Locate every Plasmodium ovale-infected red blood cell.
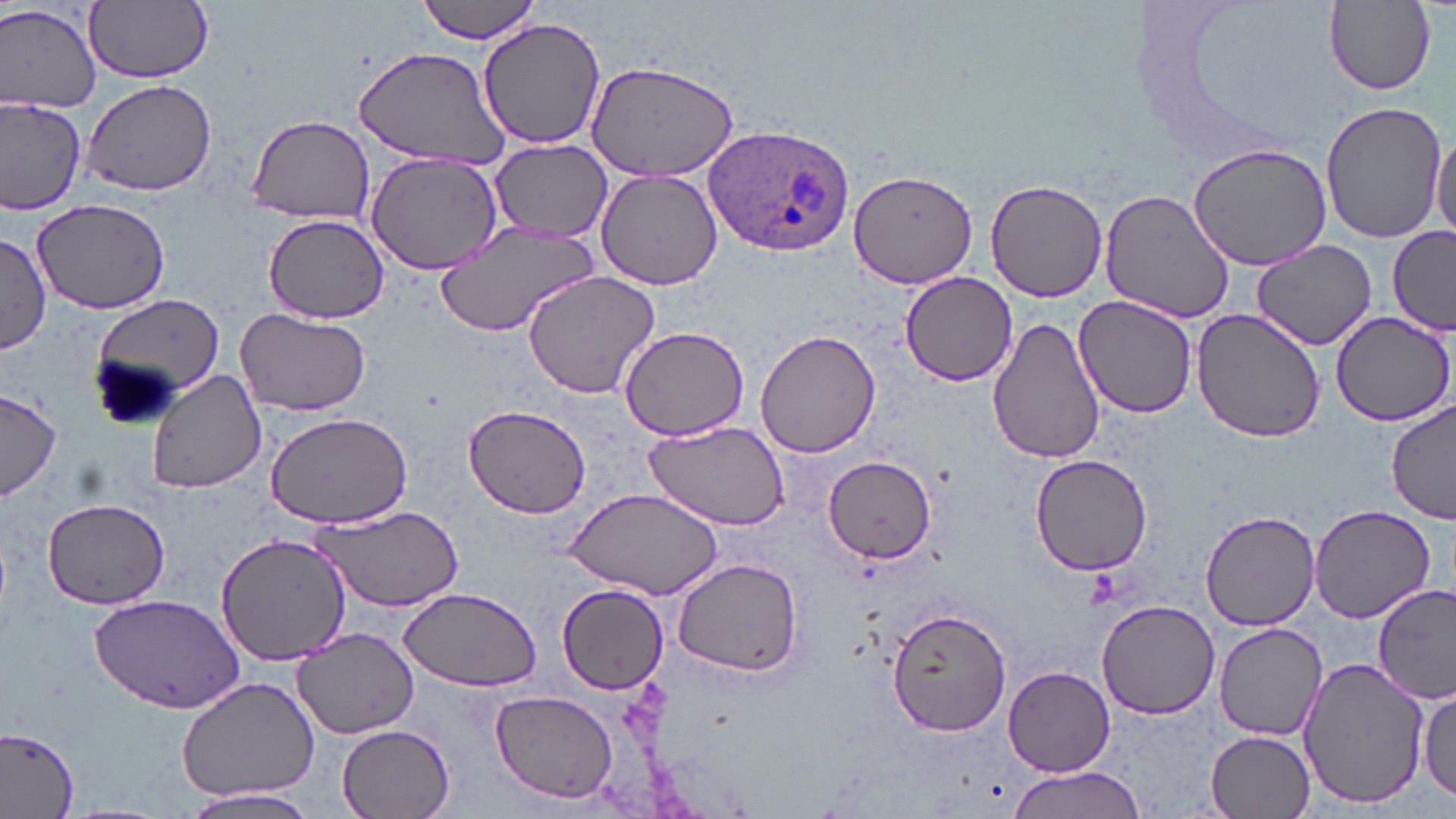
Approximate bounding boxes as (x1, y1, x2, y2) in pixels.
Plasmodium ovale-infected red blood cells: (705, 124, 857, 258).

slide-level diagnosis = Plasmodium ovale
image size = 1456×819 pixels
field of view = single
uninfected red blood cell locations = approximate bounding boxes as (x1, y1, x2, y2) in pixels: (416, 0, 548, 44), (85, 1, 213, 83), (1325, 3, 1438, 95), (0, 4, 102, 113), (476, 18, 606, 151), (354, 45, 514, 171), (585, 61, 742, 182), (79, 78, 218, 198), (0, 95, 85, 214), (1320, 101, 1446, 245), (246, 113, 375, 225), (1431, 129, 1455, 243), (488, 139, 614, 240), (1189, 143, 1330, 271), (365, 151, 503, 275), (596, 169, 724, 289), (849, 169, 980, 289), (985, 178, 1107, 301), (1099, 188, 1235, 322), (32, 198, 168, 314), (263, 214, 388, 324), (434, 219, 599, 338), (1387, 227, 1455, 336), (0, 232, 50, 354), (1248, 239, 1381, 351), (522, 268, 663, 399), (900, 271, 1018, 387), (91, 292, 224, 414), (1072, 296, 1201, 422), (233, 305, 369, 417), (1191, 309, 1325, 444), (1330, 311, 1455, 424), (988, 315, 1106, 466), (618, 324, 750, 441), (756, 329, 881, 459), (147, 370, 268, 496), (0, 388, 62, 503), (1386, 401, 1455, 525), (463, 403, 591, 519), (263, 410, 413, 529), (642, 421, 789, 529), (1028, 453, 1154, 576), (821, 455, 937, 563), (562, 486, 725, 600), (41, 498, 169, 608), (1309, 505, 1436, 623), (312, 506, 464, 610), (1202, 511, 1318, 631), (215, 533, 350, 664), (672, 558, 804, 674), (1374, 582, 1456, 702), (558, 583, 669, 694), (399, 587, 543, 692), (90, 593, 246, 713), (1097, 599, 1219, 719), (885, 606, 1014, 736), (1214, 622, 1326, 739), (292, 627, 422, 740), (1297, 656, 1430, 812), (1005, 666, 1114, 777), (175, 675, 322, 805), (1418, 684, 1456, 805), (490, 689, 619, 804), (336, 722, 456, 817), (0, 724, 79, 817), (1206, 730, 1316, 816), (1009, 766, 1146, 819), (179, 788, 323, 817)
modality = optical microscopy
stain = May-Grünwald-Giemsa
magnification = 1000x
preparation = thin blood smear